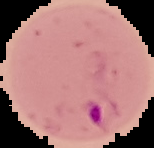
image size = 154×148 pixels
preparation = thin blood smear
result = Plasmodium parasites detected
image type = segmented cell region with the area outside set to black